Name the parasite shown.
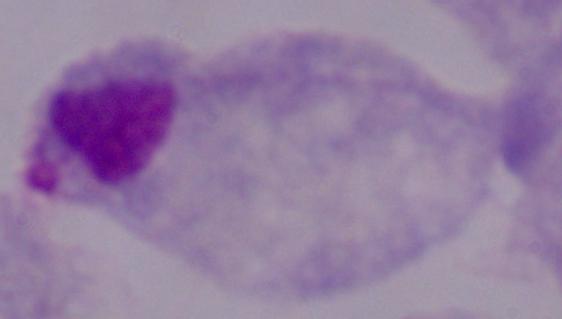

A trichomonad.

1000x magnification. Micrograph.